Locate every blood parasite and identify its species.
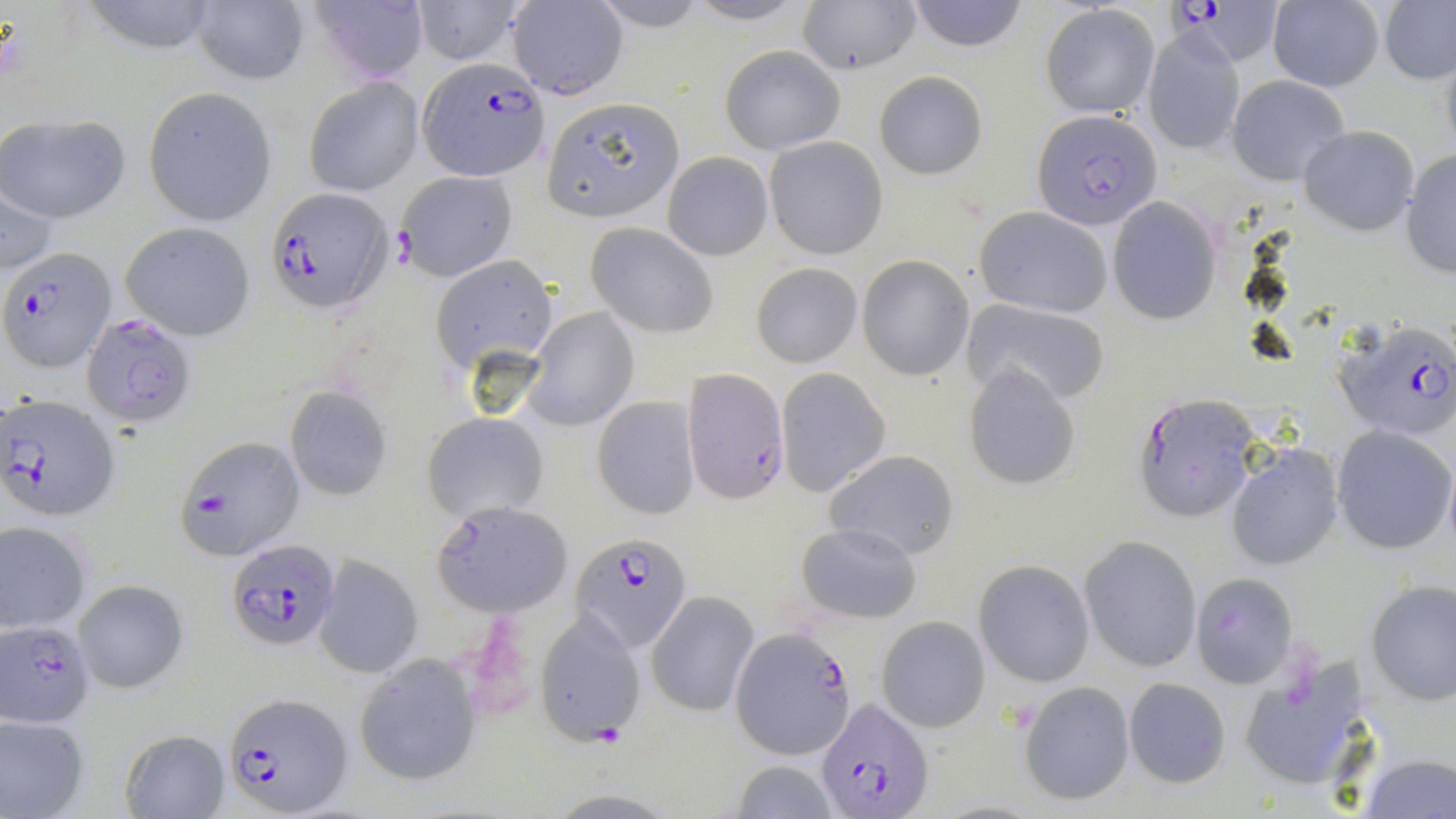

Approximate bounding boxes as (x1,y1)-(x2,y2) corner pairs in pixels.
Plasmodium falciparum-infected red blood cells: (1169,1)-(1280,66), (416,56)-(549,181), (1032,108)-(1161,228), (265,187)-(393,315), (4,248)-(117,371), (84,313)-(198,427), (1332,320)-(1456,441), (680,369)-(789,503), (1132,391)-(1261,522), (2,394)-(120,522), (574,531)-(691,652), (229,539)-(341,650), (1,620)-(96,729), (732,627)-(854,757), (221,692)-(351,817), (813,697)-(933,817).
No Plasmodium ovale, Plasmodium malariae, Plasmodium vivax, Babesia divergens, or Trypanosoma brucei observed.

Summary:
  - Uninfected red blood cell locations: (307,0)-(430,85), (408,0)-(529,66), (587,0)-(717,33), (682,0)-(816,26), (797,0)-(921,75), (905,0)-(1028,51), (1378,0)-(1456,86), (79,1)-(223,55), (506,1)-(628,100), (1265,1)-(1385,91), (188,2)-(308,87), (1040,3)-(1160,118), (1141,23)-(1247,156), (720,46)-(844,154), (875,71)-(987,180), (1226,74)-(1350,187), (303,76)-(423,198), (144,88)-(274,223), (542,97)-(684,221), (0,113)-(131,224), (1297,125)-(1420,234), (764,136)-(888,259), (1399,148)-(1456,278), (662,150)-(773,261), (395,170)-(516,281), (1,188)-(60,274), (1106,197)-(1225,325), (973,207)-(1113,319), (121,221)-(256,340), (585,222)-(718,339), (435,256)-(558,371), (858,256)-(974,379), (750,262)-(863,368), (961,299)-(1109,407), (524,306)-(639,430), (962,366)-(1082,490), (774,368)-(890,497), (285,388)-(394,499), (591,396)-(699,520), (423,412)-(547,522), (1331,425)-(1454,555), (176,434)-(305,558), (1225,444)-(1344,571), (826,450)-(958,561), (432,506)-(566,618), (792,520)-(921,624), (0,521)-(93,632), (1079,536)-(1202,673), (314,556)-(423,679), (974,560)-(1095,688), (1189,572)-(1299,689), (74,579)-(189,694), (1366,579)-(1456,705), (647,592)-(757,718), (535,610)-(646,746), (878,617)-(989,732), (1236,652)-(1367,794), (354,654)-(482,788), (1122,677)-(1231,788), (1020,681)-(1135,806), (0,711)-(90,819), (119,730)-(229,818), (1358,752)-(1454,819), (728,759)-(841,819)
  - Slide-level diagnosis: Plasmodium falciparum
  - Stain: May-Grünwald-Giemsa
  - Image size: 1456×819 pixels
  - Modality: light microscopy
  - Preparation: thin blood film
  - Field of view: single
  - Magnification: 1000x